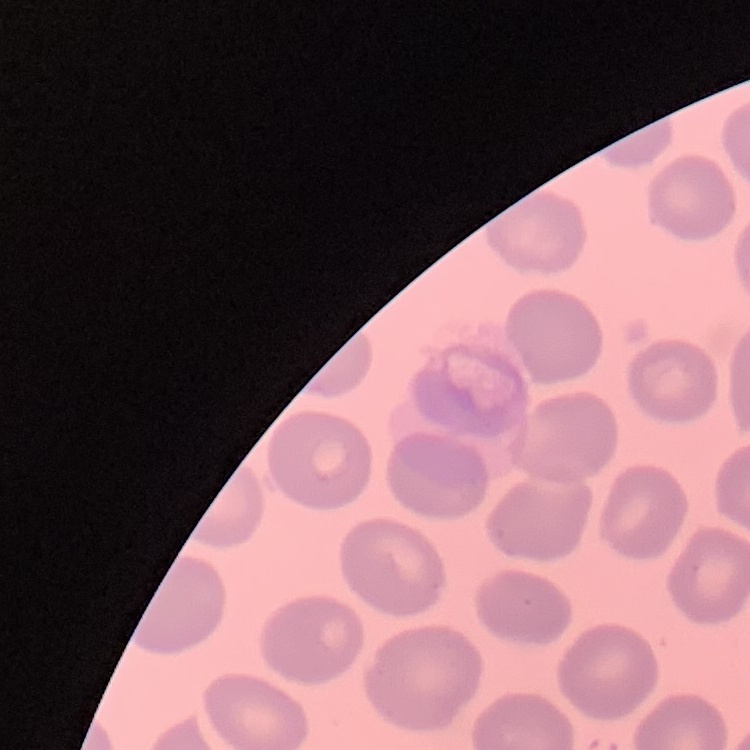
Summary:
  - Erythrocyte morphology: no rouleaux formation
  - Preparation: thin blood film
  - Image type: square crop of a larger photomicrograph
  - Stain: Field's or Giemsa